Describe the morphology of the erythrocytes.
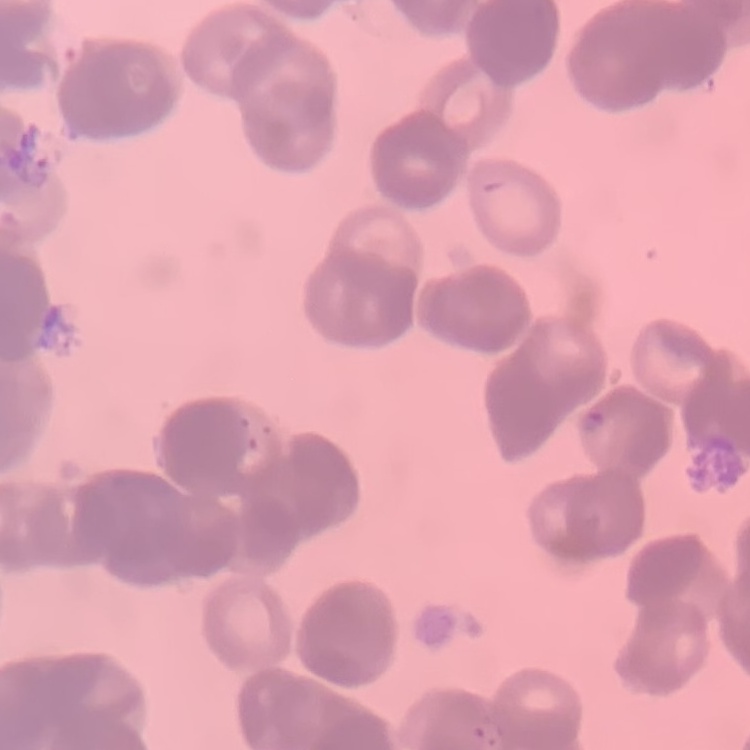

They show rouleaux formation.

One tile cut from a larger photomicrograph. Thin blood film. Stained with either Field's or Giemsa.